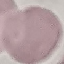

result = no malaria parasites seen
capture = smartphone camera at the microscope eyepiece
stain = Giemsa
preparation = thin smear
image type = cell patch, automatically extracted from a larger field of view and resized to 64 × 64 pixels